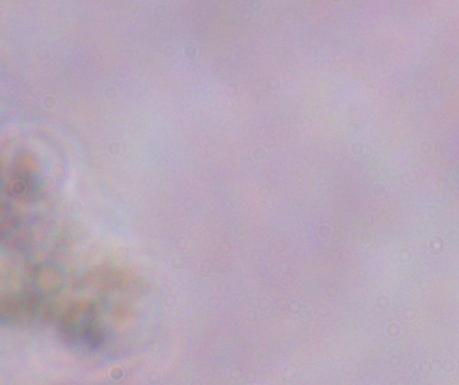
{
  "identification": "trypanosome",
  "modality": "photomicrograph",
  "magnification": "1000x"
}